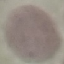

Summary:
  - Malaria status: uninfected
  - Capture: smartphone camera at the microscope eyepiece
  - Image type: automatically extracted cell patch, resized to 64 × 64 pixels
  - Stain: Giemsa
  - Preparation: thin smear